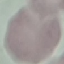 Malaria status: uninfected. Photographed with a smartphone camera at the microscope eyepiece. Giemsa-stained preparation. Automatically extracted cell patch, resized to 64 × 64 pixels. Thin smear of blood.